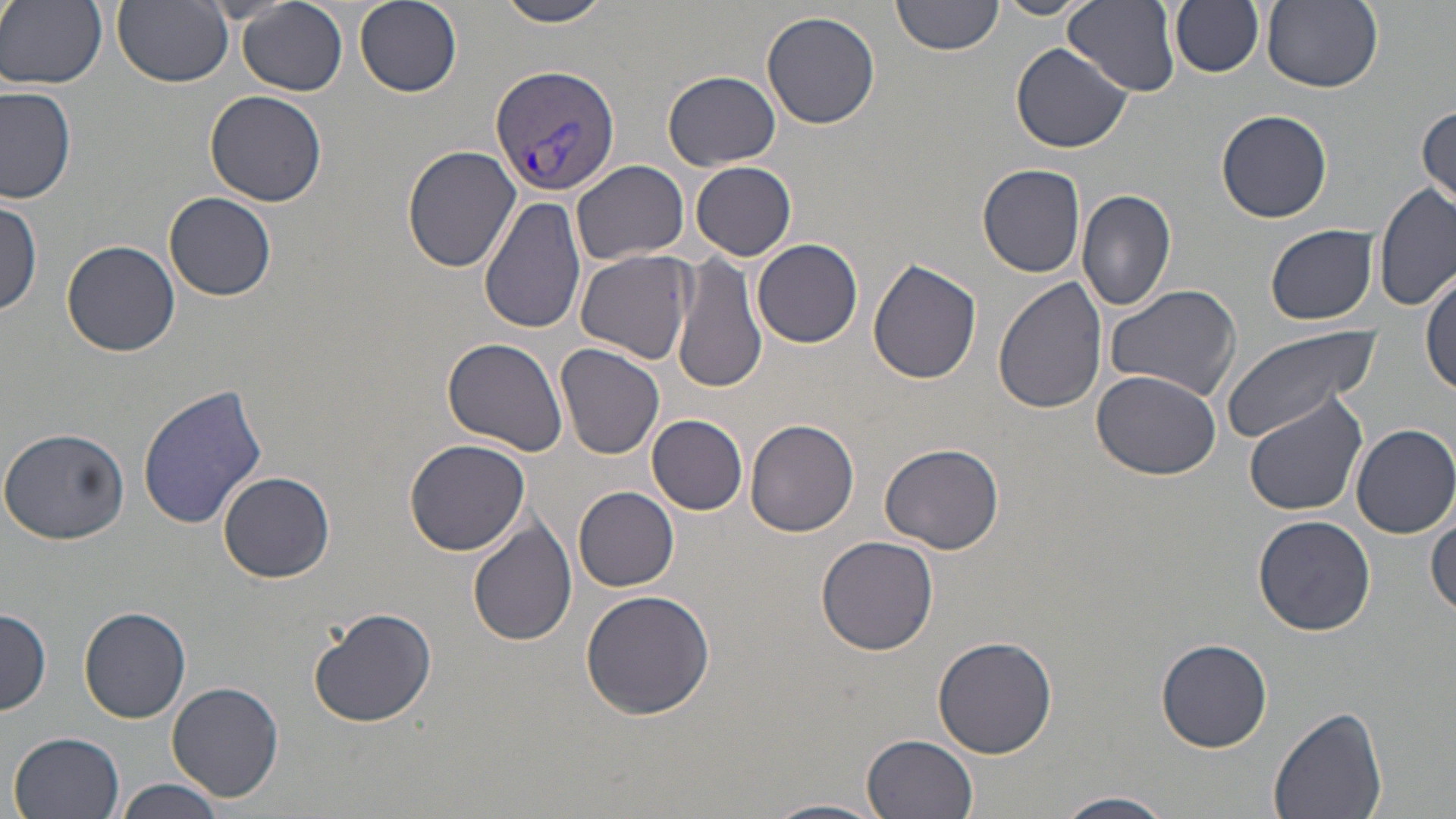
Approximate bounding boxes as (x1,y1)-(x2,y2) corner pairs in pixels. Uninfected red blood cell locations: (1,0)-(107,90), (354,0)-(461,97), (493,0)-(618,27), (893,0)-(1005,57), (1066,0)-(1180,94), (1170,0)-(1263,78), (1261,0)-(1383,93), (112,1)-(233,88), (989,1)-(1093,21), (238,2)-(347,95), (762,10)-(883,131), (1011,42)-(1131,154), (663,70)-(781,170), (0,86)-(76,204), (204,89)-(328,206), (1415,104)-(1454,211), (1216,109)-(1333,223), (403,145)-(520,272), (573,160)-(690,266), (691,161)-(797,260), (978,163)-(1087,276), (1375,184)-(1453,315), (1075,187)-(1176,312), (164,192)-(276,301), (0,195)-(44,316), (479,197)-(587,334), (1266,224)-(1379,324), (752,239)-(863,348), (61,240)-(181,356), (574,248)-(695,366), (672,251)-(767,396), (868,260)-(982,385), (1422,267)-(1454,401), (992,278)-(1106,415), (1102,281)-(1244,404), (1220,326)-(1386,441), (443,337)-(569,458), (556,342)-(666,459), (1090,366)-(1225,479), (137,385)-(269,530), (1241,394)-(1368,516), (647,415)-(748,515), (745,420)-(861,538), (1352,423)-(1456,539), (0,426)-(131,544), (404,436)-(531,555), (880,441)-(1004,554), (219,470)-(336,583), (574,487)-(679,592), (1428,509)-(1456,618), (1253,515)-(1376,636), (468,519)-(577,647), (815,535)-(939,655), (580,589)-(717,721), (0,607)-(51,718), (79,607)-(192,724), (308,607)-(438,728), (931,636)-(1058,757), (1156,639)-(1273,753), (167,682)-(285,802), (1268,704)-(1388,819), (9,731)-(126,819), (861,733)-(978,818), (115,777)-(228,819), (1056,792)-(1178,818), (764,799)-(890,819). Plasmodium vivax-infected red blood cell locations: (490,66)-(624,196). Slide-level diagnosis: Plasmodium vivax. Light microscopy. Thin blood film. May-Grünwald-Giemsa-stained preparation. Captured at 1000x magnification. Image is 1456×819 pixels. Single field of view.